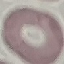
malaria status = uninfected
capture = smartphone through the microscope eyepiece
stain = Giemsa
image type = cell patch, automatically extracted from a larger field of view and resized to 64 × 64 pixels
preparation = thin blood film